Name the parasite shown.
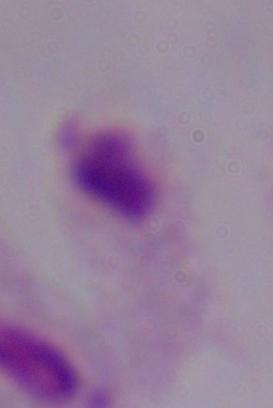
This is a trichomonad.

Captured at 1000x magnification. Photomicrograph.